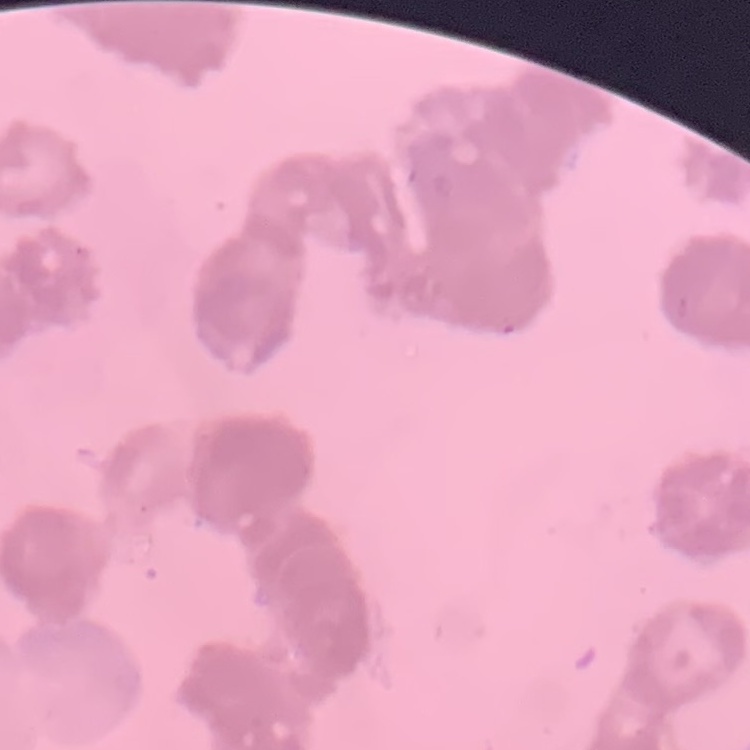
red blood cell morphology = rouleaux formation
stain = Field's or Giemsa
image type = one tile cut from a larger photomicrograph
preparation = thin blood film